Comment on the morphology of the erythrocytes.
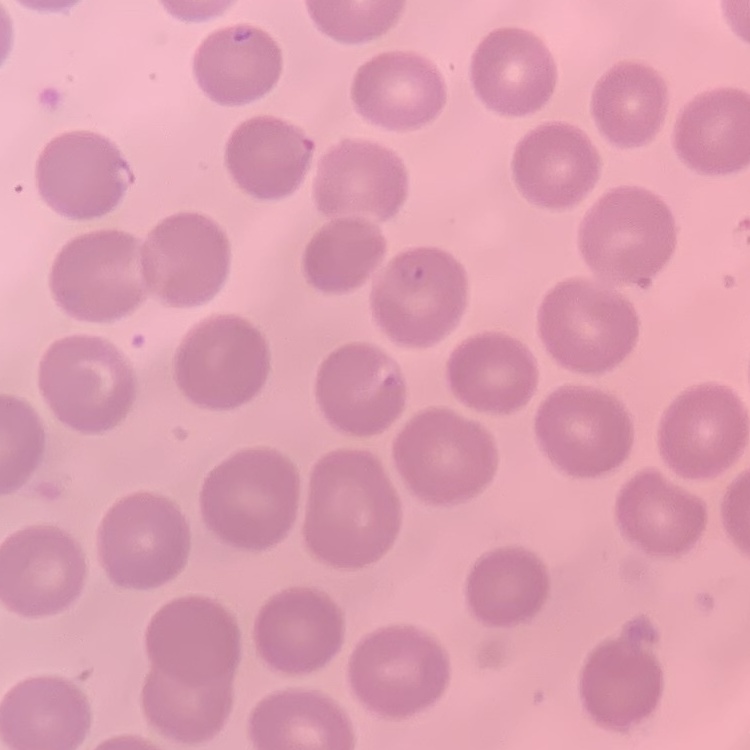
No rouleaux formation.

Summary:
  - Preparation: thin blood smear
  - Stain: Field's or Giemsa
  - Image type: one tile cut from a larger photomicrograph